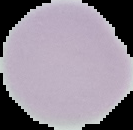
Summary:
  - Image type: segmented cell region on a black background
  - Result: negative for Plasmodium parasites
  - Image size: 133×130 pixels
  - Preparation: thin blood smear